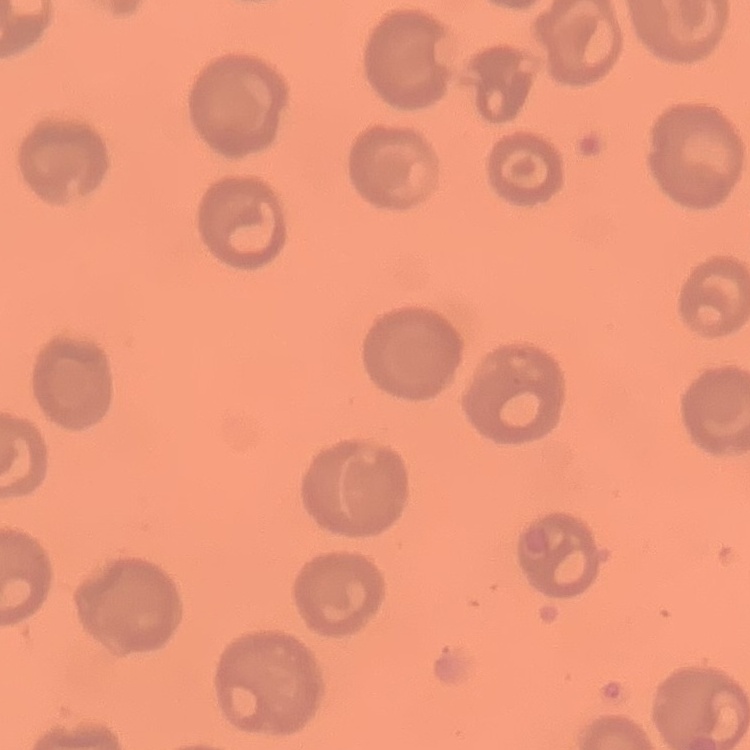
The red blood cells exhibit no rouleaux formation. Field's or Giemsa stain. Thin blood film. One tile cut from a larger photomicrograph.